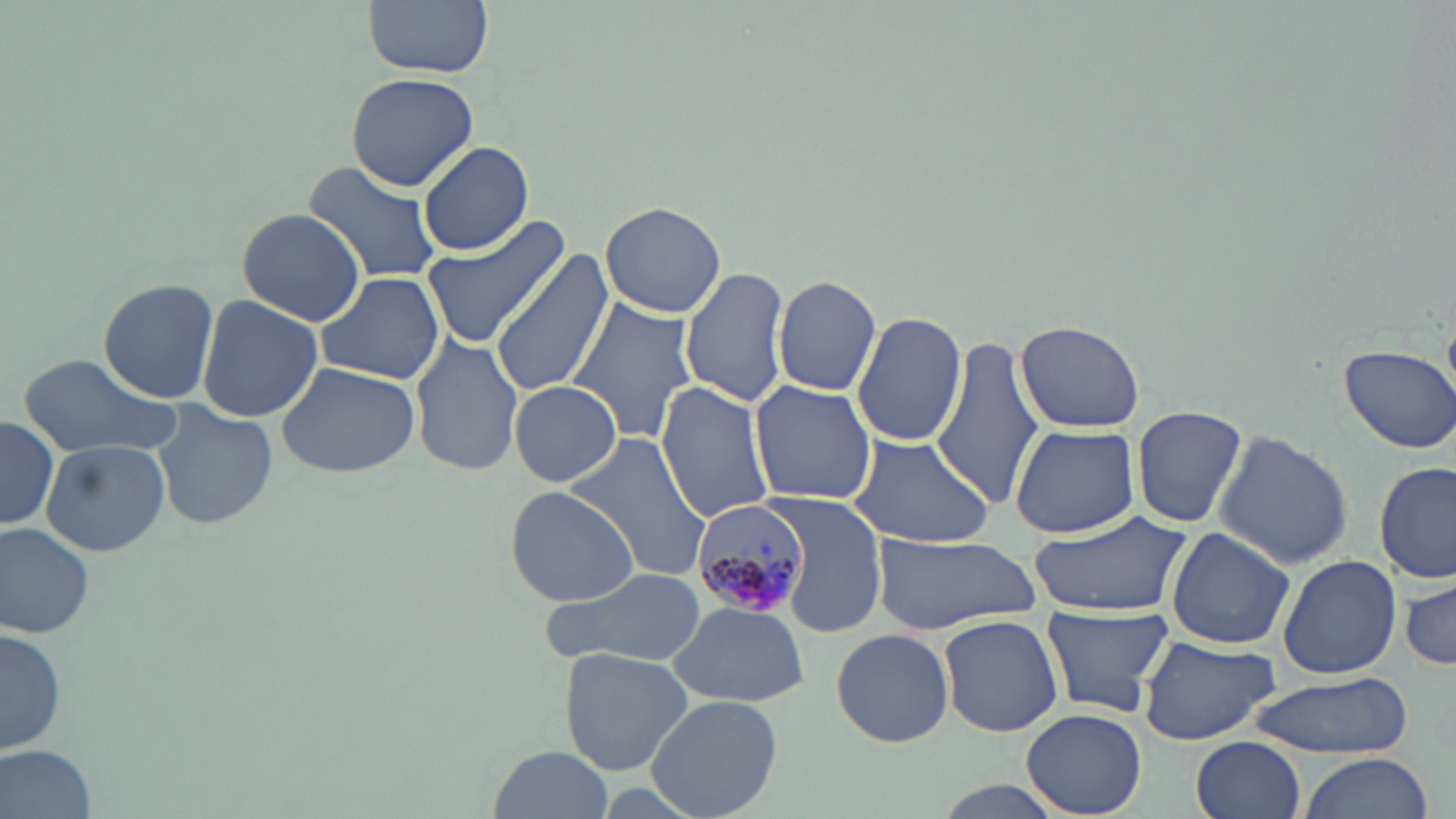
Summary:
  - Coordinate format: approximate bounding boxes as (x1, y1, x2, y2) in pixels
  - Plasmodium malariae-infected red blood cell locations: (691, 500, 810, 618)
  - Uninfected red blood cell locations: (364, 0, 495, 78), (345, 69, 480, 192), (416, 140, 534, 256), (303, 159, 445, 286), (601, 200, 728, 317), (235, 207, 367, 327), (420, 216, 573, 348), (489, 250, 614, 396), (680, 265, 792, 408), (313, 271, 444, 387), (772, 275, 880, 396), (96, 277, 220, 403), (196, 294, 322, 423), (568, 297, 700, 442), (851, 311, 966, 446), (1015, 319, 1146, 432), (933, 331, 1045, 508), (409, 333, 522, 476), (1337, 343, 1456, 454), (18, 355, 182, 461), (274, 360, 422, 479), (509, 380, 621, 487), (748, 380, 877, 503), (656, 382, 776, 523), (152, 401, 276, 533), (1131, 405, 1248, 529), (1, 415, 60, 531), (1010, 425, 1138, 538), (844, 430, 998, 548), (561, 431, 712, 586), (1213, 432, 1354, 571), (40, 438, 170, 557), (1376, 461, 1456, 585), (505, 486, 639, 605), (771, 496, 886, 637), (1026, 511, 1191, 617), (0, 520, 98, 638), (1167, 525, 1295, 650), (871, 534, 1040, 634), (1278, 555, 1400, 679), (538, 565, 709, 669), (1399, 577, 1456, 671), (666, 601, 808, 707), (1041, 604, 1173, 719), (939, 614, 1063, 738), (2, 627, 67, 754), (831, 628, 955, 748), (1136, 634, 1281, 747), (561, 648, 693, 774), (1245, 671, 1412, 759), (647, 693, 782, 818), (1023, 708, 1146, 816), (1190, 737, 1305, 819), (2, 744, 98, 817), (487, 746, 613, 819), (1295, 754, 1435, 819), (930, 780, 1066, 817)
  - Slide-level diagnosis: Plasmodium malariae
  - Stain: May-Grünwald-Giemsa
  - Modality: light microscopy
  - Field of view: single
  - Magnification: 1000x
  - Image size: 1456×819 pixels
  - Preparation: thin blood smear